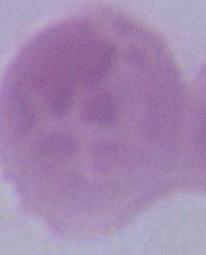

Captured at 1000x magnification. A red blood cell is seen. Photomicrograph.